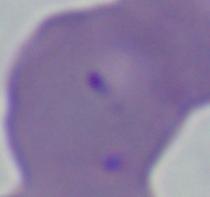

magnification: 1000x
identification: Babesia
modality: photomicrograph